Name the parasite shown.
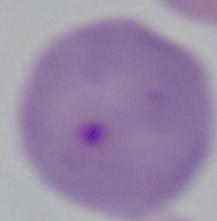
Babesia.

magnification = 1000x
modality = photomicrograph